State which cell type is depicted.
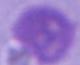

An erythrocyte.

Captured at 1000x magnification. Micrograph.